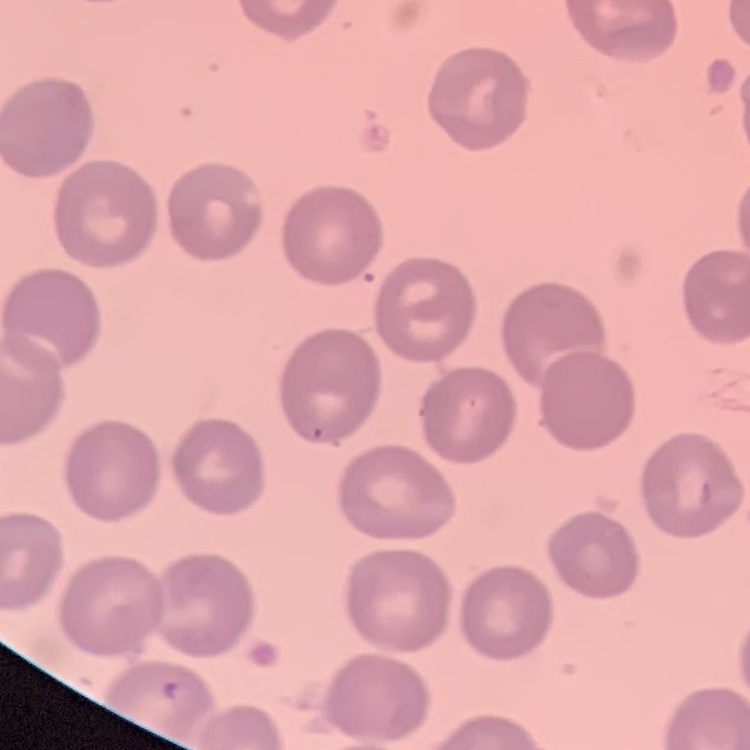

Summary:
  - Erythrocyte morphology: no rouleaux formation
  - Preparation: thin blood smear
  - Stain: Field's or Giemsa
  - Image type: square crop of a larger photomicrograph